State which cell type is depicted.
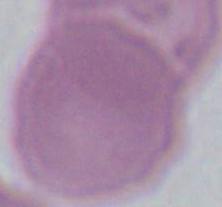

This is an erythrocyte.

Micrograph. Captured at 1000x magnification.